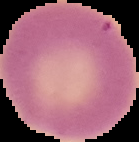

Summary:
  - Image type: cell region segmented out of the field of view; surrounding area masked to black
  - Image size: 139×142 pixels
  - Result: negative for malaria parasites
  - Preparation: thin blood smear